Locate every leukocyte (white blood cell).
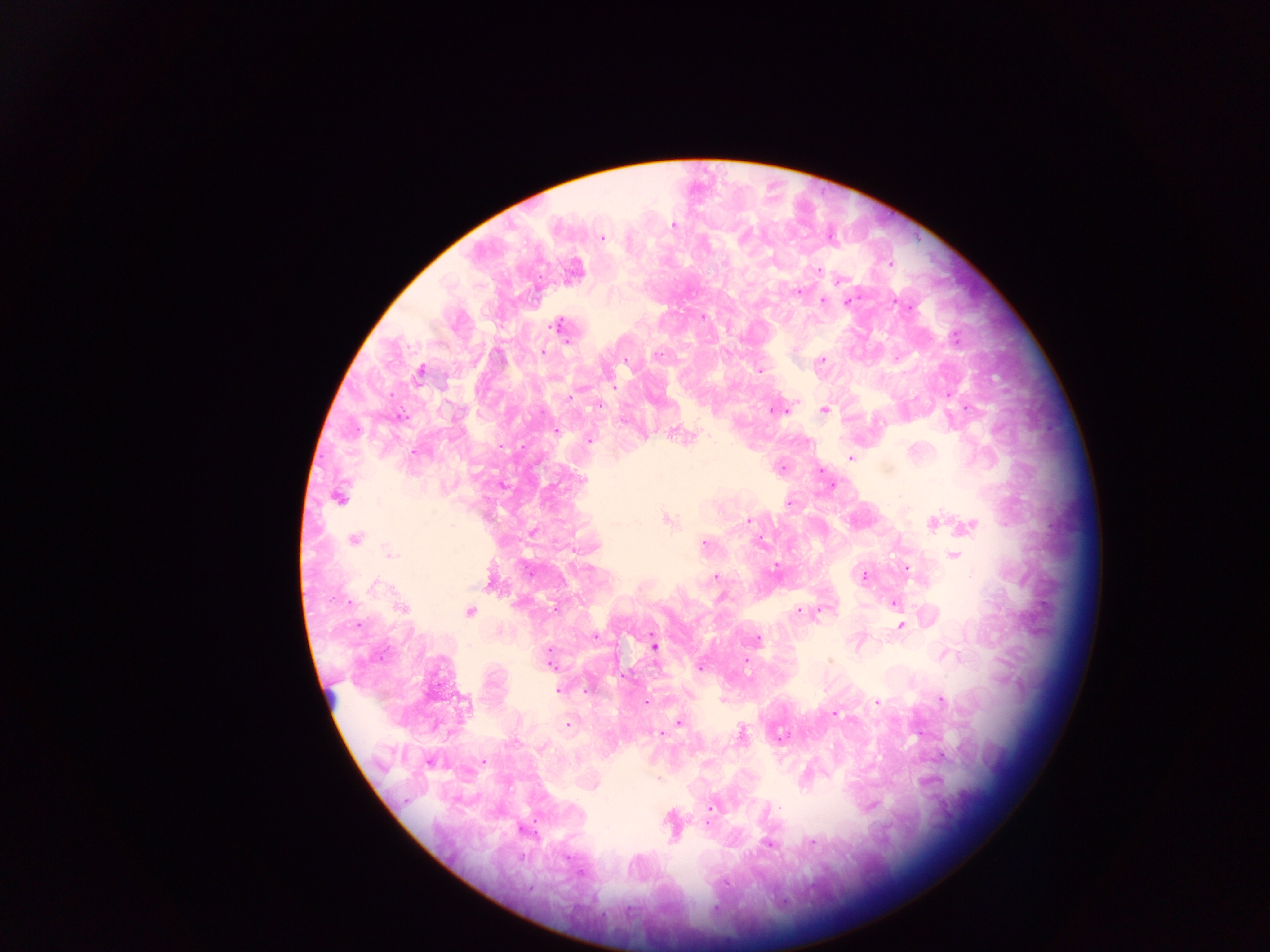

Approximate centers as [x, y] in pixels.
Leukocytes (some below the resolvable threshold): [333, 694].

Malaria parasite locations: [673, 224], [601, 238], [724, 263], [890, 263], [818, 272], [841, 279], [798, 293], [823, 300], [848, 301], [703, 316], [557, 326], [955, 338], [795, 349], [542, 353], [499, 355], [657, 355], [823, 359], [626, 361], [759, 370], [419, 372], [613, 387], [571, 397], [598, 406], [790, 406], [776, 410], [785, 410], [823, 410], [556, 431], [589, 440], [416, 452], [851, 458], [781, 468], [582, 480], [339, 498], [789, 503], [668, 521], [748, 521], [932, 522], [968, 526], [354, 540], [761, 540], [704, 544], [391, 554], [954, 556], [776, 566], [909, 570], [864, 576], [716, 577], [376, 586], [895, 604], [401, 608], [798, 610], [470, 611], [820, 611], [901, 626], [595, 636], [758, 638], [654, 646], [946, 654], [746, 660], [828, 660], [550, 664], [700, 667], [558, 690], [588, 690], [722, 700], [941, 701], [646, 702], [877, 702], [466, 703], [835, 714], [680, 723], [567, 724], [741, 733], [662, 734], [780, 737], [483, 761], [431, 762], [657, 779], [780, 807], [710, 808], [811, 841], [768, 843], [726, 883]. Thick blood smear. Single field of view. Image is 1270×952 pixels. Sample from Ghana. Mobile-phone photograph taken through the microscope.